Point out each Plasmodium parasite and classify it by life-cycle stage.
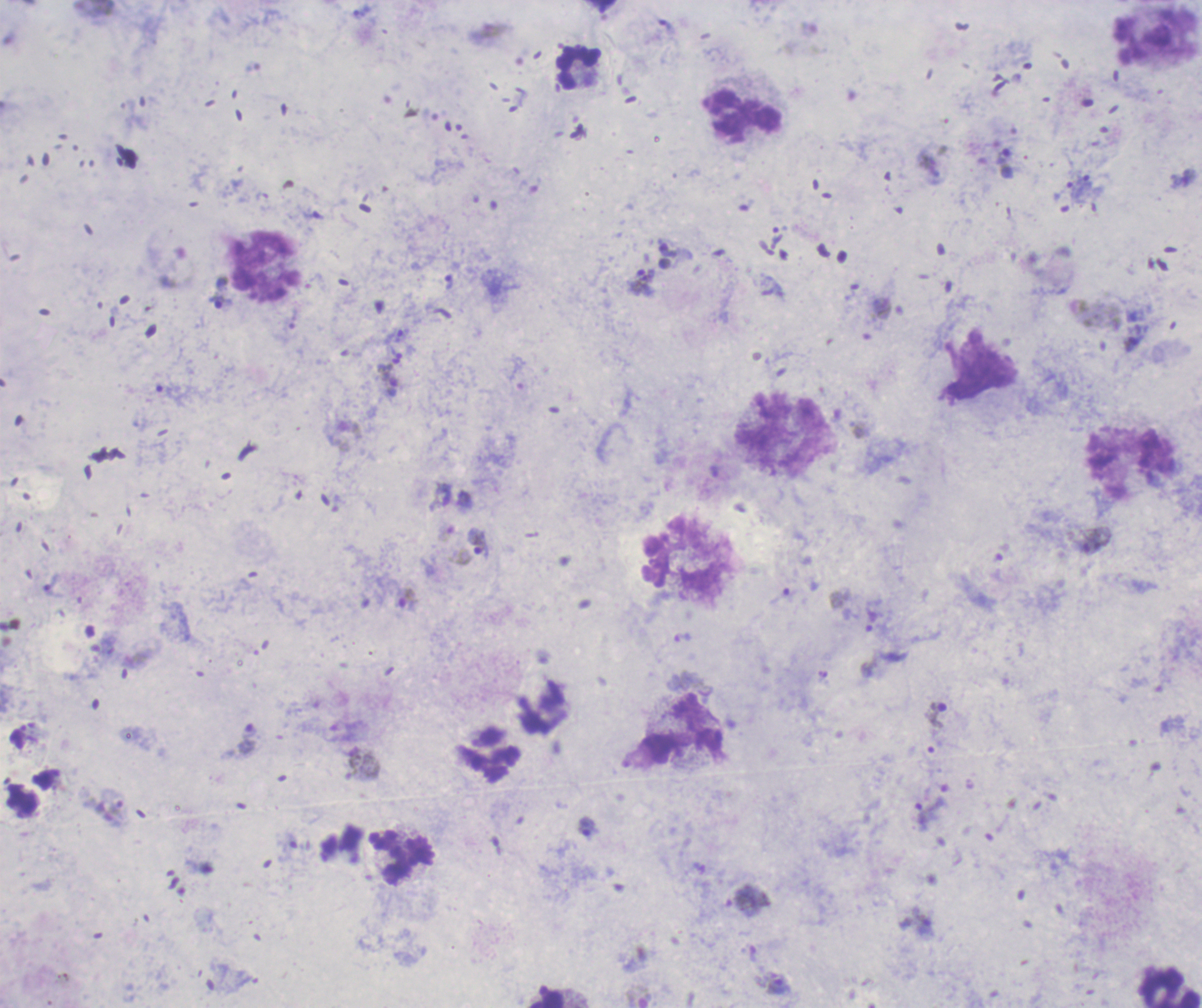
Approximate centers as {x, y} in pixels.
Trophozoites: {642, 282}, {219, 301}, {388, 380}, {478, 543}, {407, 599}, {871, 621}, {938, 715}, {248, 740}, {363, 768}, {589, 827}, {924, 924}, {777, 984}.
No schizont or gametocyte forms observed.

Approximate centers as {x, y} in pixels. Leukocyte locations: {578, 68}, {742, 116}, {266, 267}, {784, 432}, {1131, 462}, {686, 560}, {684, 728}, {490, 756}, {401, 857}, {1160, 986}. Captured at 100x magnification. Previously used in an actual diagnosis. Romanowsky-stained preparation. One field from this slide. Background quality: satisfactory. Image is 1202×1008 pixels. Thick blood smear.